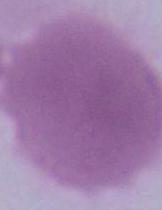

Summary:
  - Identification: red blood cell
  - Modality: micrograph
  - Magnification: 1000x